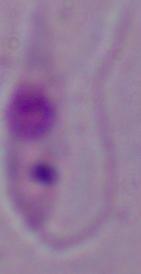
{
  "identification": "Leishmania",
  "modality": "photomicrograph",
  "magnification": "1000x"
}